Assess this cell for malaria.
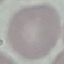

Uninfected.

capture: smartphone camera at the microscope eyepiece
preparation: thin blood smear
stain: Giemsa
image_type: automatically extracted cell patch, resized to 64 × 64 pixels